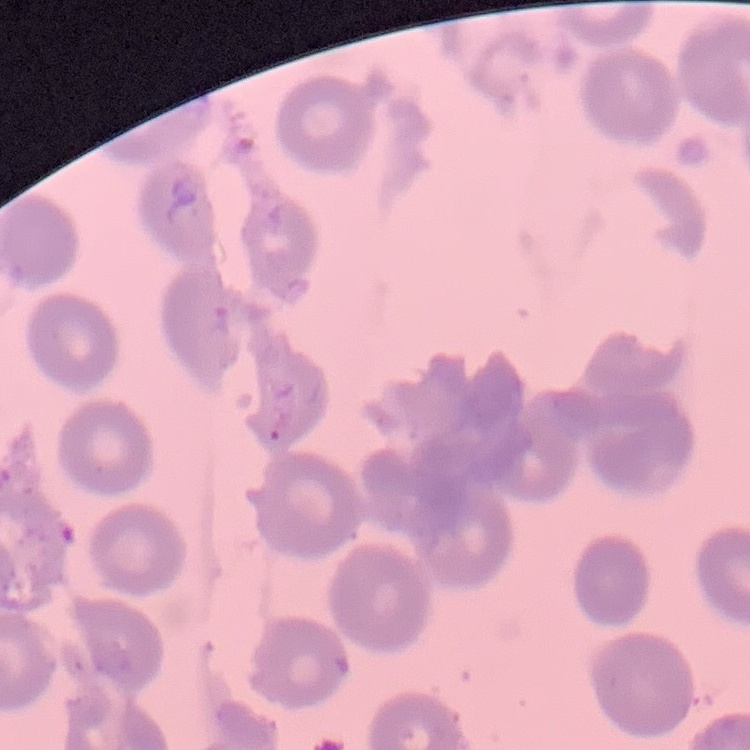

The red blood cells show no rouleaux formation. Square crop of a larger photomicrograph. Thin blood smear. Field's or Giemsa stain.